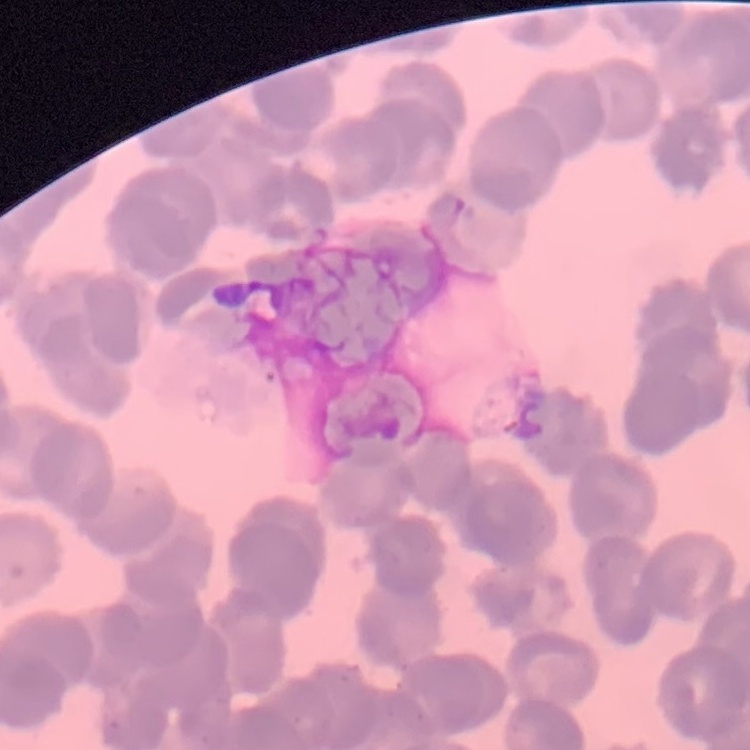 The erythrocytes exhibit rouleaux formation. Square crop of a larger photomicrograph. Thin blood film. Field's or Giemsa stain.